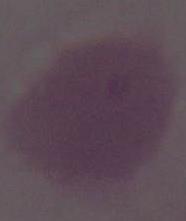
Summary:
  - Identification: red blood cell
  - Magnification: 1000x
  - Modality: photomicrograph